Identify the cell.
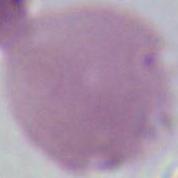

An erythrocyte.

modality = photomicrograph
magnification = 1000x